Identify the parasite.
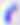
Toxoplasma gondii.

Summary:
  - Magnification: 400x
  - Modality: micrograph